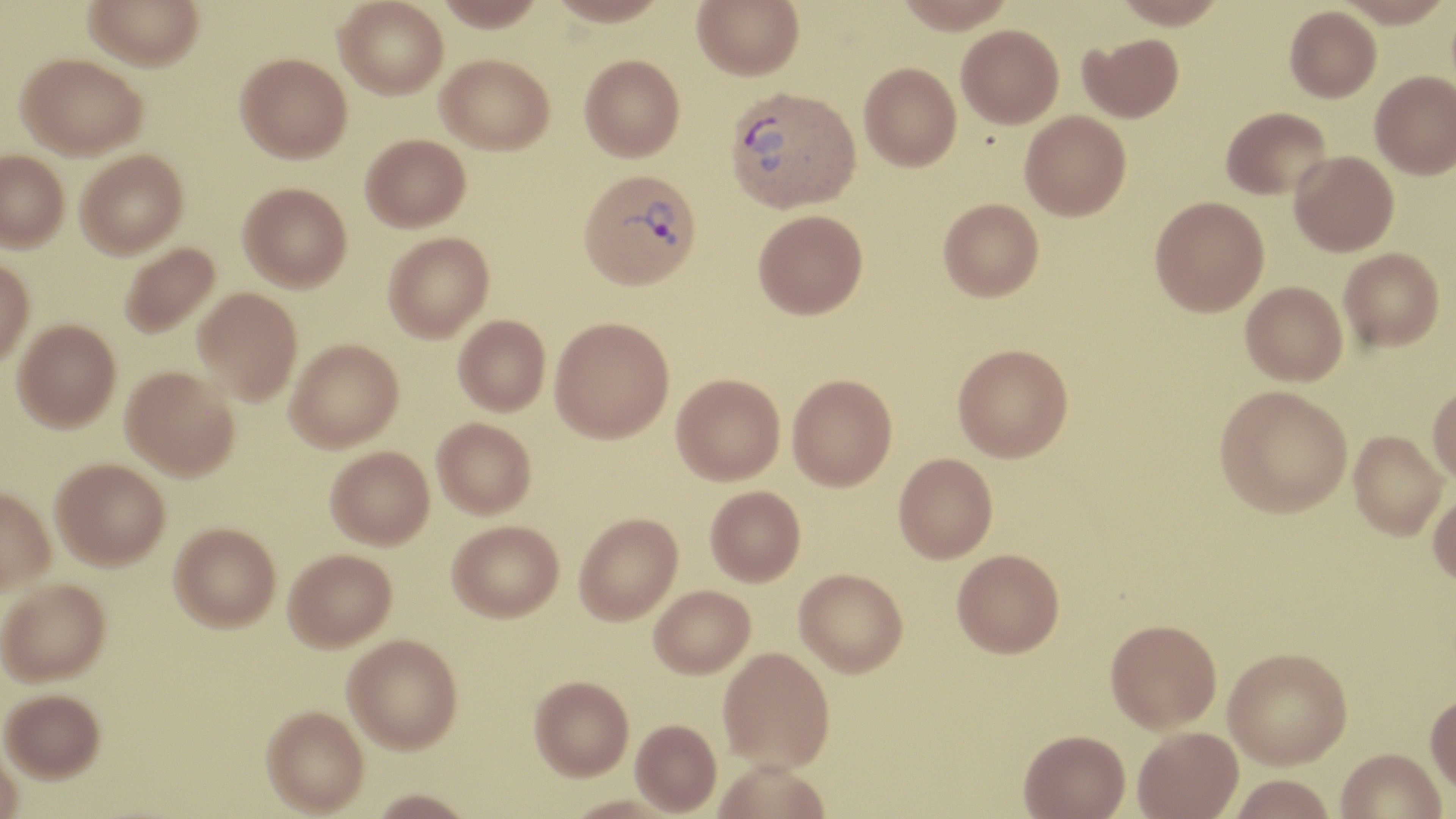

slide-level diagnosis = Plasmodium vivax
preparation = thin blood smear
field of view = single
stain = May-Grünwald-Giemsa
image size = 1456×819 pixels
modality = light microscopy
magnification = 1000x
Plasmodium vivax-infected red blood cell locations = approximate bounding boxes as (x1,y1)-(x2,y2) corner pairs in pixels: (724,85)-(861,213), (578,168)-(702,290)
uninfected red blood cell locations = approximate bounding boxes as (x1,y1)-(x2,y2) corner pairs in pixels: (83,0)-(205,70), (334,0)-(448,99), (436,0)-(546,31), (548,0)-(669,27), (692,0)-(804,80), (892,0)-(1016,34), (1112,0)-(1226,29), (1333,0)-(1452,27), (1285,5)-(1381,102), (956,25)-(1063,128), (1079,33)-(1184,123), (235,52)-(351,162), (17,53)-(147,160), (436,54)-(554,154), (579,54)-(685,161), (859,62)-(961,171), (1370,71)-(1456,178), (1221,107)-(1331,200), (1020,110)-(1131,221), (360,134)-(470,231), (75,149)-(188,258), (0,150)-(69,252), (1289,150)-(1399,256), (239,182)-(352,292), (1149,196)-(1269,316), (938,198)-(1043,300), (752,209)-(867,319), (383,232)-(494,342), (118,242)-(221,339), (1338,248)-(1444,352), (0,256)-(35,368), (1241,280)-(1347,385), (193,287)-(303,405), (453,315)-(550,415), (549,316)-(674,443), (12,319)-(121,432), (285,338)-(404,452), (952,343)-(1073,462), (121,365)-(240,481), (671,373)-(785,484), (787,374)-(897,491), (1427,381)-(1456,484), (1214,384)-(1352,517), (432,417)-(536,518), (1348,430)-(1448,539), (325,445)-(434,549), (894,452)-(997,562), (51,457)-(170,570), (0,485)-(56,594), (705,486)-(806,587), (1428,486)-(1456,586), (574,513)-(683,626), (447,520)-(563,622), (169,521)-(281,631), (283,548)-(397,652), (952,550)-(1064,661), (794,570)-(908,679), (0,578)-(111,687), (649,586)-(755,679), (1104,621)-(1221,736), (343,635)-(463,754), (718,649)-(836,775), (1224,650)-(1352,772), (529,676)-(633,782), (1,688)-(105,782), (1425,693)-(1456,797), (261,706)-(368,815), (631,721)-(722,815), (1133,729)-(1243,819), (1018,733)-(1130,819), (0,740)-(23,819), (1334,750)-(1446,819), (711,763)-(830,819), (1227,777)-(1337,819), (367,789)-(479,818)